Point out each Plasmodium parasite.
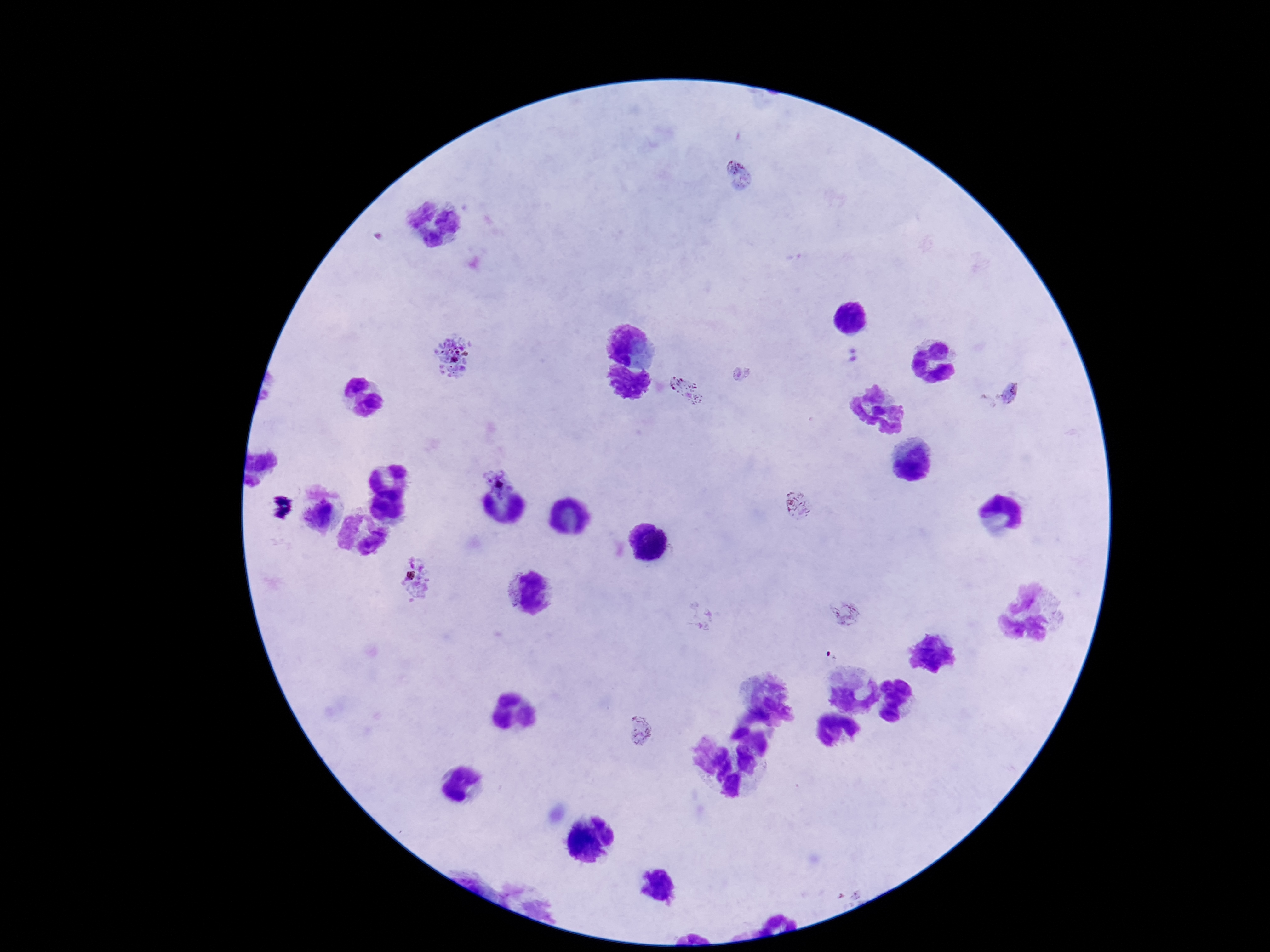
Approximate centers as (x, y) in pixels.
Plasmodium parasites: (738, 174), (851, 354), (452, 355), (741, 374), (686, 391), (1011, 393), (498, 481), (800, 507), (416, 580), (1049, 598), (846, 613), (1058, 620), (639, 733).

patient malaria status = positive
capture = smartphone camera through the microscope eyepiece
magnification = 100x
image size = 1270×952 pixels
field of view = single
stain = Giemsa
preparation = thick blood smear